Assess for malaria.
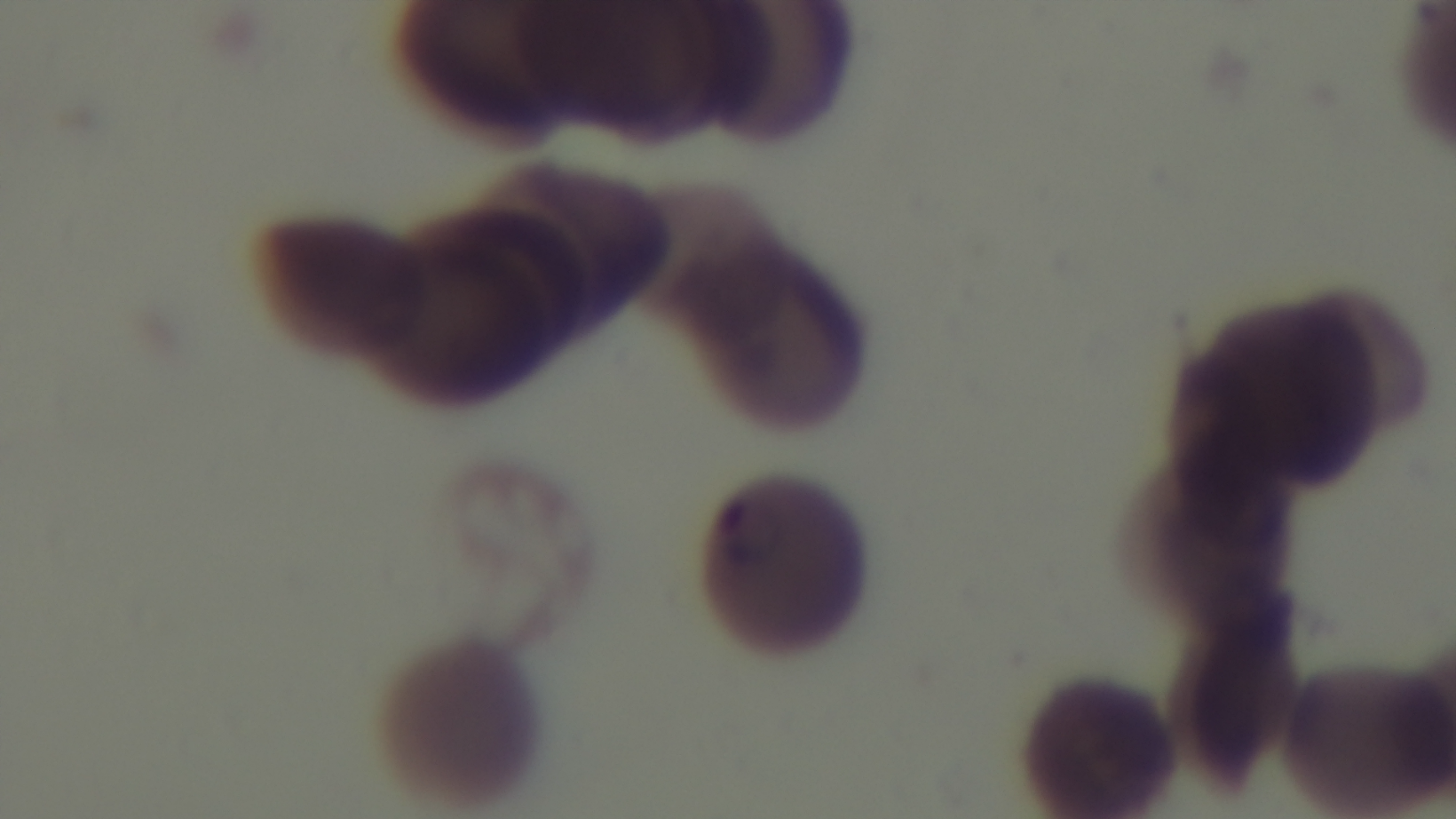

Infected.

modality: light microscopy
stain: Giemsa
field_of_view: single
preparation: thin
objective: 100x oil immersion
capture: mounted 4K digital camera